Locate every Plasmodium parasite and every leukocyte.
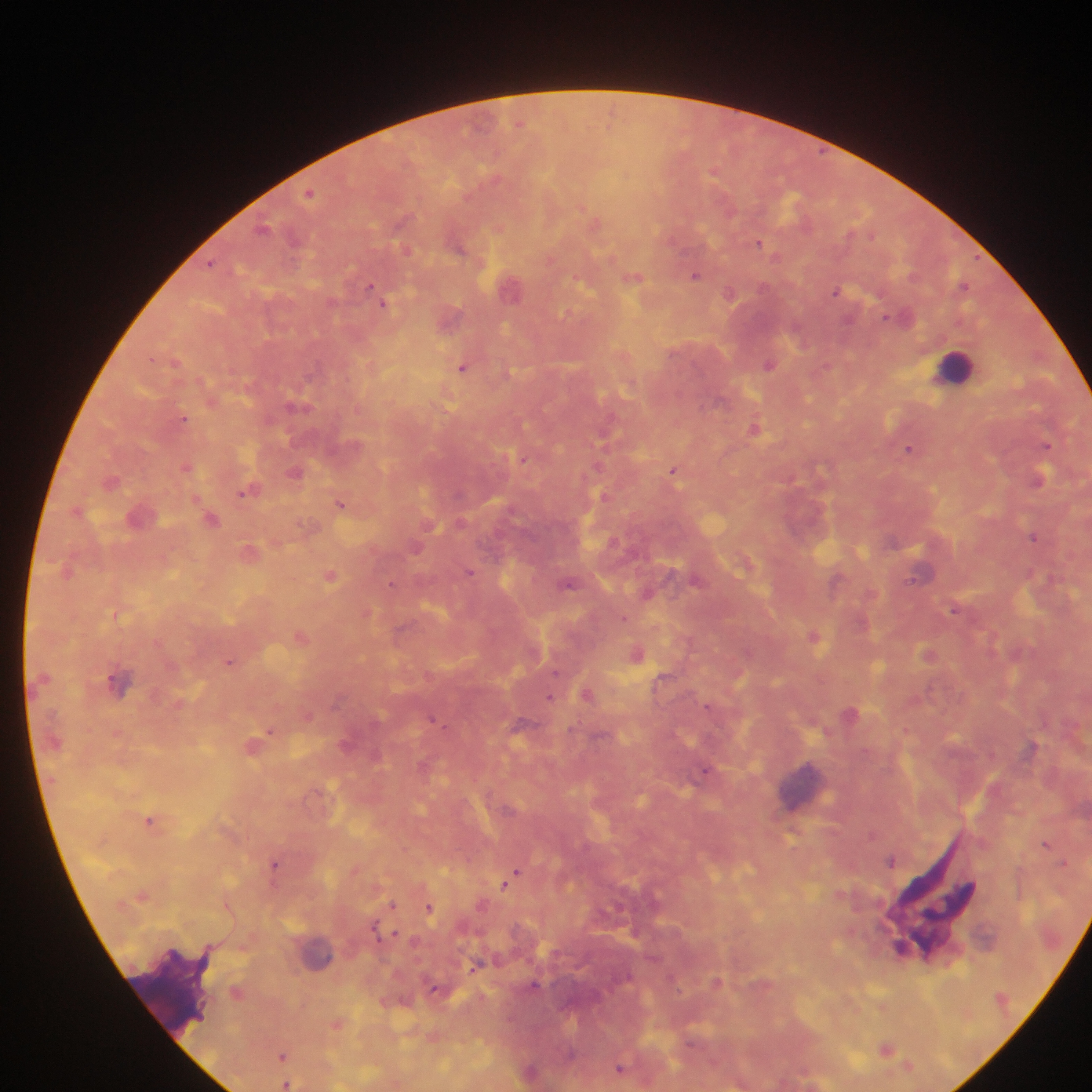
Approximate centers as (x, y) in pixels.
Plasmodium parasites: (519, 123), (713, 173), (309, 193), (262, 227), (759, 242), (407, 249), (211, 263), (694, 276), (635, 278), (963, 286), (369, 287), (512, 288), (836, 290), (730, 293), (384, 304), (886, 316), (769, 365), (463, 368), (295, 406), (183, 418), (755, 429), (603, 436), (1047, 445), (908, 449), (523, 458), (187, 467), (673, 470), (295, 472), (1039, 479), (111, 481), (244, 492), (341, 504), (211, 519), (1033, 537), (469, 571), (920, 573), (330, 576), (696, 579), (392, 584), (568, 584), (647, 593), (955, 609), (813, 635), (637, 655), (230, 662), (555, 671), (587, 695), (550, 696), (708, 706), (434, 719), (269, 731), (1031, 747), (704, 770), (149, 821), (870, 834), (1046, 843), (891, 860), (274, 863), (1063, 864), (514, 873), (507, 883), (392, 903), (429, 908), (374, 927), (395, 933), (534, 985), (434, 988), (887, 1048), (570, 1055), (282, 1056), (908, 1066), (620, 1067), (286, 1084).
Leukocytes: (955, 365), (803, 784), (321, 954).

preparation = thick blood smear
capture = mobile-phone photograph through a microscope
field of view = single
image size = 1092×1092 pixels
country = Ghana